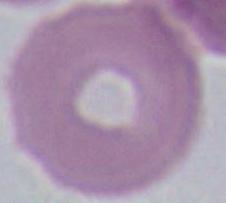
identification: erythrocyte
modality: micrograph
magnification: 1000x